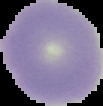
image_type: cell region segmented out of the field of view; surrounding area masked to black
result: no malaria parasites detected
image_size: 103×106 pixels
preparation: thin blood smear